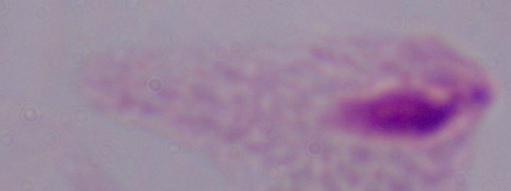

Summary:
  - Identification: trichomonad
  - Magnification: 1000x
  - Modality: photomicrograph